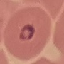

result: malaria parasites detected
capture: smartphone camera at the microscope eyepiece
image_type: automatically extracted cell patch, resized to 64 × 64 pixels
stain: Giemsa
preparation: thin smear